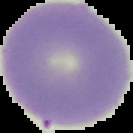

Summary:
  - Preparation: thin blood smear
  - Image type: segmented cell region with the area outside set to black
  - Image size: 133×133 pixels
  - Malaria status: uninfected